Assess this cell for malaria.
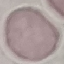
It is uninfected.

Giemsa stain. Acquired by smartphone through the microscope eyepiece. Automatically extracted cell patch, resized to 64 × 64 pixels. Thin smear of blood.